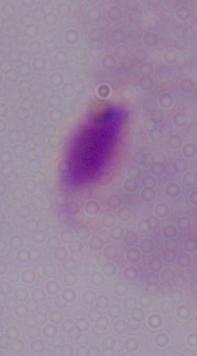
Summary:
  - Modality: photomicrograph
  - Magnification: 1000x
  - Identification: trichomonad